State which parasite is depicted.
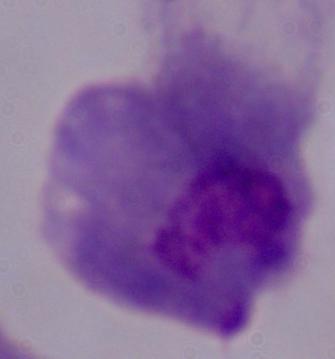

A trichomonad.

1000x magnification. Micrograph.